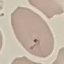

Summary:
  - Malaria status: parasitized
  - Preparation: thin blood smear
  - Stain: Giemsa
  - Capture: smartphone camera at the microscope eyepiece
  - Image type: automatically extracted cell patch, resized to 64 × 64 pixels